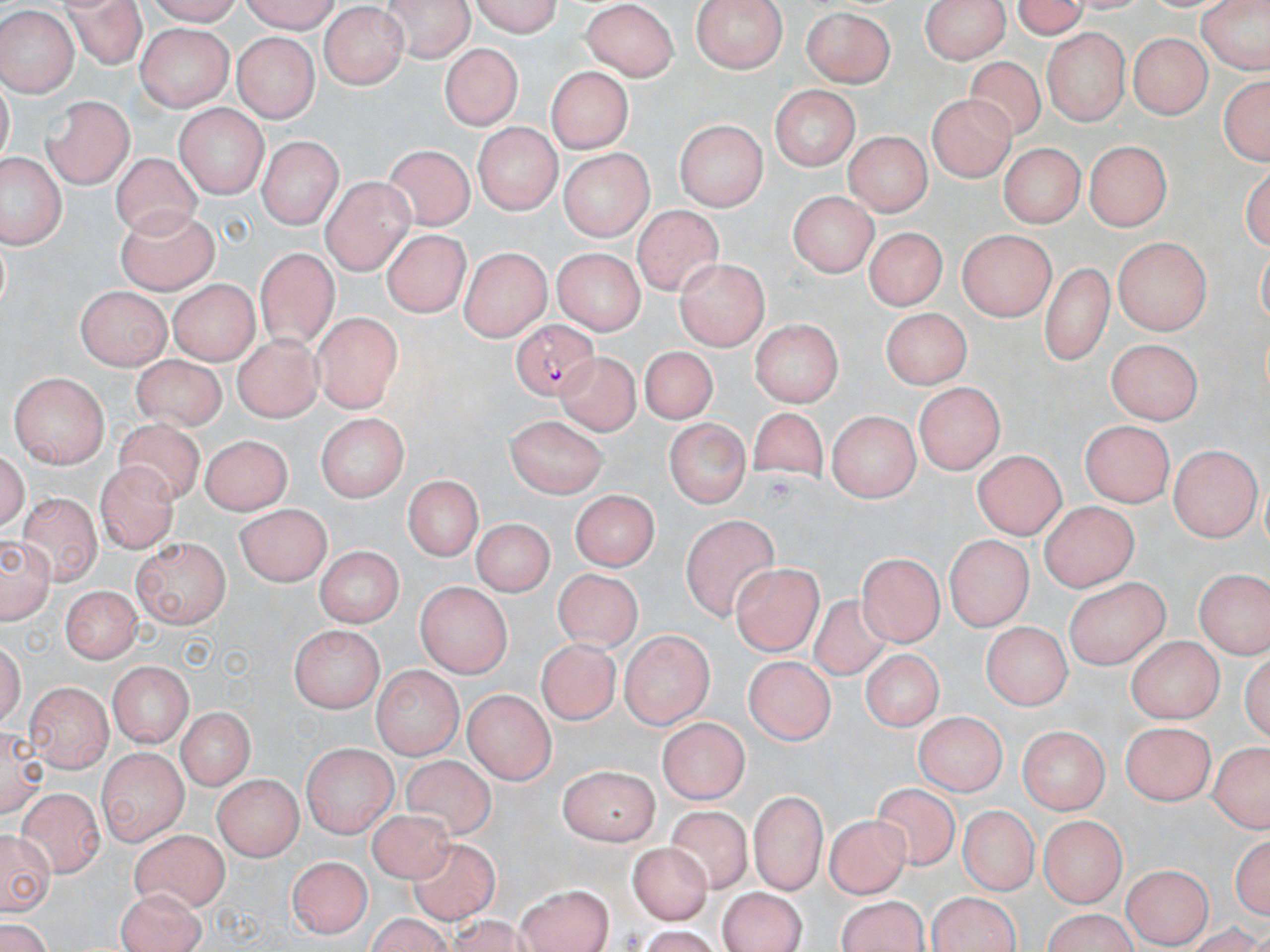

slide-level diagnosis = Plasmodium falciparum
uninfected red blood cell locations = approximate bounding boxes as (x1,y1)-(x2,y2) corner pairs in pixels: (63,0)-(145,64), (237,0)-(341,29), (382,0)-(474,61), (465,0)-(562,35), (688,0)-(785,73), (924,0)-(1006,66), (1005,0)-(1096,38), (1199,0)-(1267,80), (583,2)-(677,81), (320,7)-(410,89), (800,8)-(899,85), (0,10)-(74,95), (136,24)-(235,109), (1041,30)-(1131,125), (1128,32)-(1212,120), (231,34)-(320,120), (439,41)-(521,131), (964,54)-(1048,144), (548,66)-(635,153), (1216,70)-(1269,170), (769,85)-(861,167), (928,93)-(1017,183), (43,94)-(136,187), (175,102)-(270,197), (674,119)-(765,210), (475,123)-(558,214), (846,132)-(931,215), (1085,139)-(1173,227), (258,140)-(340,228), (998,141)-(1082,229), (386,145)-(475,231), (556,150)-(654,240), (112,153)-(199,237), (2,154)-(60,246), (319,177)-(415,271), (790,189)-(875,277), (118,205)-(219,293), (632,206)-(724,295), (865,227)-(943,312), (380,230)-(471,318), (954,230)-(1057,317), (1113,236)-(1213,333), (257,247)-(334,341), (460,247)-(550,340), (549,247)-(644,334), (675,256)-(772,345), (1039,261)-(1116,359), (166,280)-(257,363), (76,285)-(171,369), (882,308)-(970,392), (313,312)-(401,414), (749,321)-(845,404), (233,333)-(318,424), (1107,339)-(1202,424), (641,346)-(714,424), (561,349)-(644,440), (128,353)-(225,432), (11,374)-(110,467), (913,384)-(1003,473), (749,406)-(827,485), (829,409)-(921,499), (319,415)-(405,503), (506,416)-(609,499), (664,418)-(749,508), (115,420)-(201,511), (1079,421)-(1177,508), (203,432)-(294,514), (1167,448)-(1257,540), (971,450)-(1068,537), (97,464)-(182,554), (404,473)-(482,558), (571,491)-(657,574), (18,492)-(101,584), (1039,502)-(1136,589), (235,503)-(332,586), (681,516)-(783,618), (470,517)-(556,594), (0,531)-(56,626), (946,535)-(1030,631), (130,538)-(230,630), (312,545)-(405,625), (858,553)-(940,646), (733,564)-(820,655), (552,566)-(639,650), (1194,568)-(1268,660), (1063,576)-(1169,668), (57,583)-(142,665), (414,583)-(512,679), (809,593)-(891,683), (983,621)-(1072,707), (289,625)-(386,709), (620,629)-(712,730), (1128,635)-(1220,723), (535,641)-(621,725), (862,652)-(942,732), (743,656)-(835,744), (105,660)-(191,746), (371,669)-(463,757), (25,682)-(111,772), (465,689)-(554,784), (173,707)-(258,790), (913,709)-(1004,795), (658,714)-(746,805), (1119,724)-(1213,808), (1020,729)-(1108,814), (305,740)-(396,839), (1206,740)-(1269,835), (100,747)-(188,844), (403,755)-(495,843), (558,761)-(658,844), (212,773)-(301,860), (871,781)-(959,870), (16,785)-(106,876), (746,788)-(826,891), (961,807)-(1035,894), (667,808)-(755,897), (368,809)-(460,888), (823,814)-(912,896), (1038,814)-(1125,904), (0,827)-(58,915), (132,827)-(226,911), (1233,835)-(1269,923), (407,839)-(500,923), (627,840)-(706,924), (288,856)-(368,937), (1120,863)-(1210,946), (513,885)-(613,952), (718,886)-(806,952), (111,889)-(205,951), (930,892)-(1023,952), (837,896)-(929,952), (1038,909)-(1142,952)
field of view = single
preparation = thin blood film
modality = light microscopy
Plasmodium falciparum-infected red blood cell locations = approximate bounding boxes as (x1,y1)-(x2,y2) corner pairs in pixels: (513,319)-(596,400)
magnification = 1000x
stain = May-Grünwald-Giemsa
image size = 1270×952 pixels